Name the parasite shown.
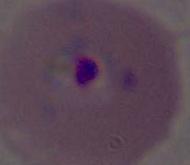

This is Plasmodium.

Summary:
  - Magnification: 400x or 1000x
  - Modality: micrograph